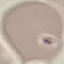
result = no malaria parasites detected
capture = smartphone camera at the microscope eyepiece
preparation = thin blood smear
image type = cell patch, automatically extracted from a larger field of view and resized to 64 × 64 pixels
stain = Giemsa